Name the parasite shown.
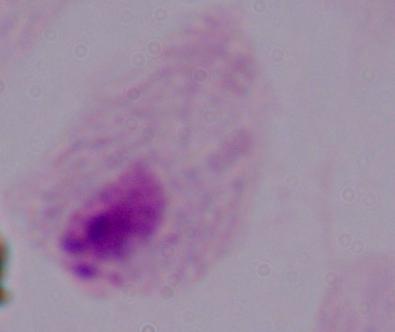
A trichomonad.

modality = micrograph
magnification = 1000x